Report the malaria status of this cell.
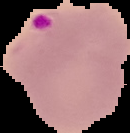

It is parasitized.

From a thin blood smear. Image is 130×133 pixels. Segmented cell region on a black background.